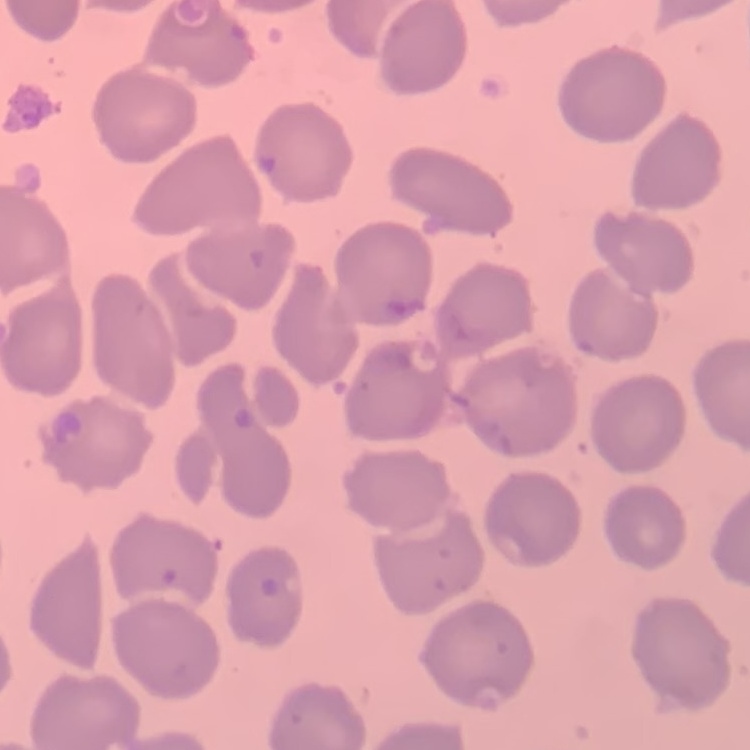
red blood cell morphology = no rouleaux formation
preparation = thin blood smear
image type = one tile cut from a larger photomicrograph
stain = Field's or Giemsa